Name the blood parasite species.
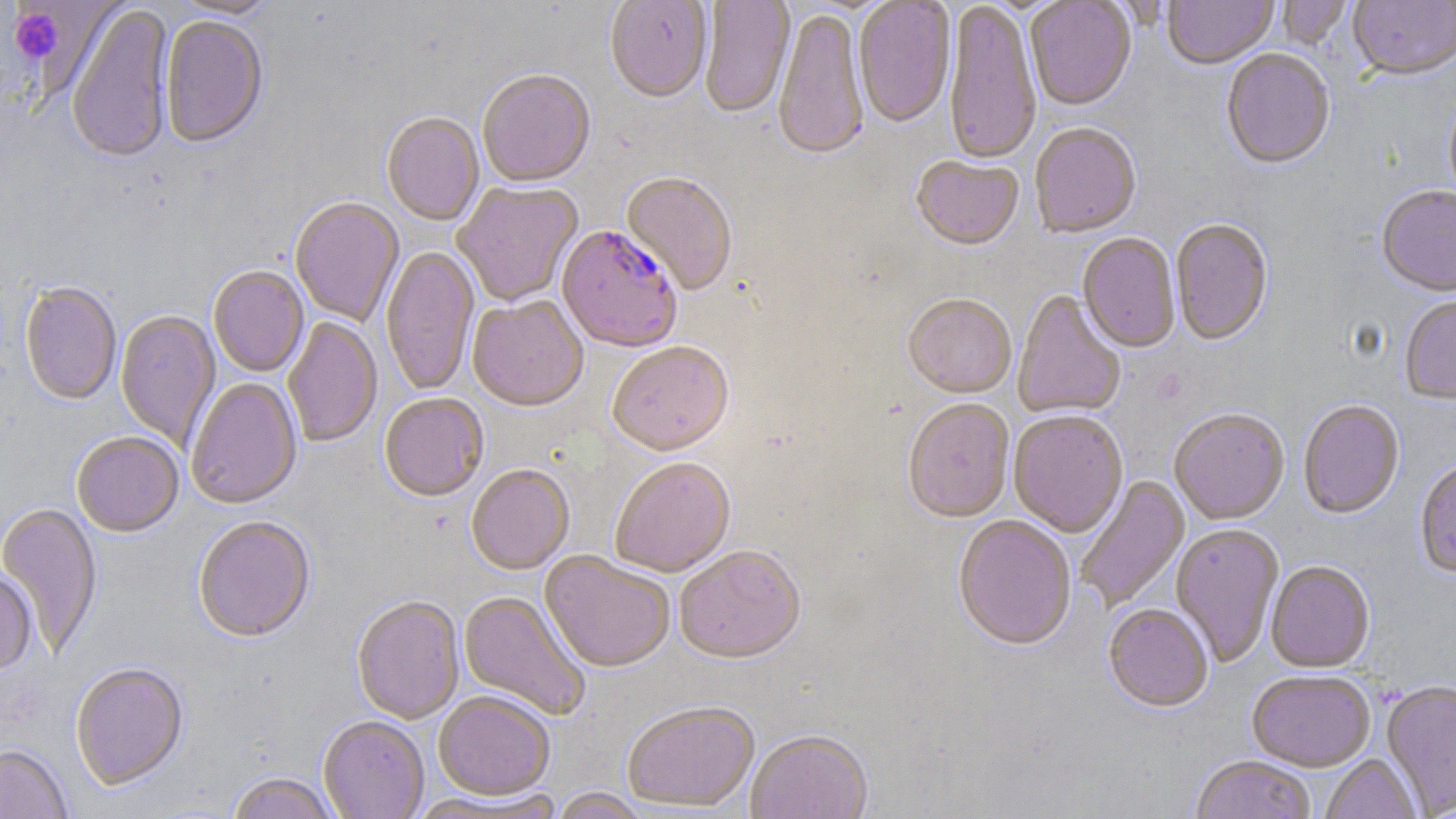

Plasmodium falciparum.

Approximate bounding boxes as (x1, y1, x2, y2) in pixels. Platelet locations: (8, 8, 63, 62). Plasmodium falciparum-infected red blood cell locations: (556, 227, 682, 355). Uninfected red blood cell locations: (169, 0, 279, 20), (605, 0, 712, 105), (699, 0, 795, 120), (854, 0, 956, 131), (944, 0, 1042, 170), (1025, 0, 1137, 113), (1163, 0, 1278, 71), (1276, 1, 1354, 52), (1349, 1, 1456, 83), (67, 5, 174, 167), (773, 10, 870, 164), (161, 18, 268, 151), (1221, 50, 1336, 172), (477, 72, 595, 190), (1444, 90, 1456, 214), (381, 113, 484, 228), (1029, 125, 1141, 241), (910, 157, 1024, 253), (620, 173, 738, 297), (452, 182, 584, 308), (1376, 188, 1456, 299), (290, 197, 405, 328), (1170, 220, 1273, 347), (1078, 235, 1180, 354), (381, 246, 480, 397), (208, 267, 309, 378), (19, 282, 121, 406), (1012, 291, 1126, 420), (903, 296, 1016, 400), (467, 297, 589, 414), (1400, 298, 1456, 407), (116, 310, 221, 450), (283, 318, 383, 449), (608, 344, 734, 460), (186, 378, 302, 512), (379, 395, 489, 504), (902, 400, 1015, 525), (1298, 401, 1404, 520), (1008, 411, 1128, 538), (1170, 411, 1289, 527), (72, 433, 184, 538), (610, 458, 736, 579), (1414, 462, 1456, 579), (466, 466, 575, 577), (1076, 475, 1190, 613), (0, 503, 102, 657), (193, 517, 316, 645), (952, 517, 1077, 654), (1170, 524, 1284, 667), (674, 548, 806, 667), (539, 551, 675, 674), (1267, 562, 1375, 674), (0, 572, 37, 672), (457, 590, 592, 722), (352, 597, 465, 725), (1103, 605, 1213, 714), (70, 664, 189, 792), (1247, 672, 1375, 772), (1382, 680, 1456, 818), (433, 692, 555, 801), (622, 703, 760, 813), (318, 717, 429, 818), (745, 732, 873, 819), (0, 746, 73, 819), (1321, 755, 1421, 819), (1191, 757, 1316, 819), (226, 773, 341, 819), (549, 789, 650, 819). May-Grünwald-Giemsa-stained preparation. Light microscopy. Thin blood film. One field of a larger specimen. 1000x magnification. Image is 1456×819 pixels.